Assess for malaria.
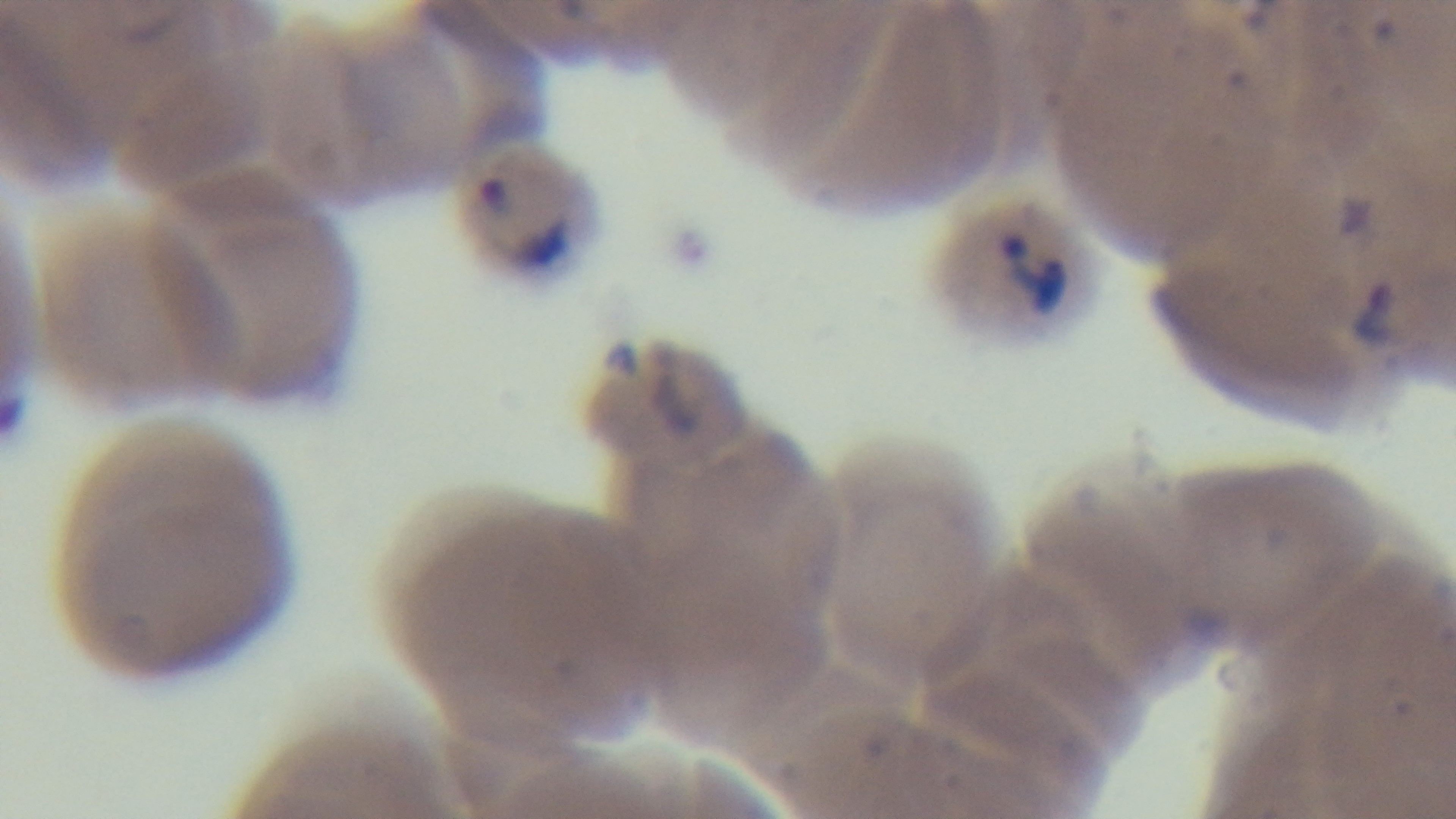
It is infected.

Preparation: thin. 100x oil-immersion objective. Mounted 4K digital camera. Photomicrograph. Single field of view. Giemsa-stained.